State which parasite is depicted.
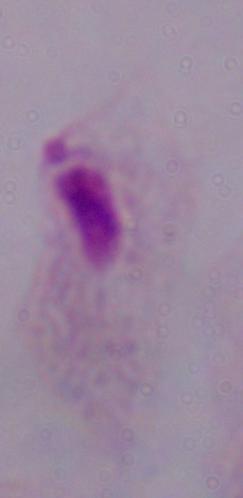

A trichomonad.

Summary:
  - Modality: micrograph
  - Magnification: 1000x